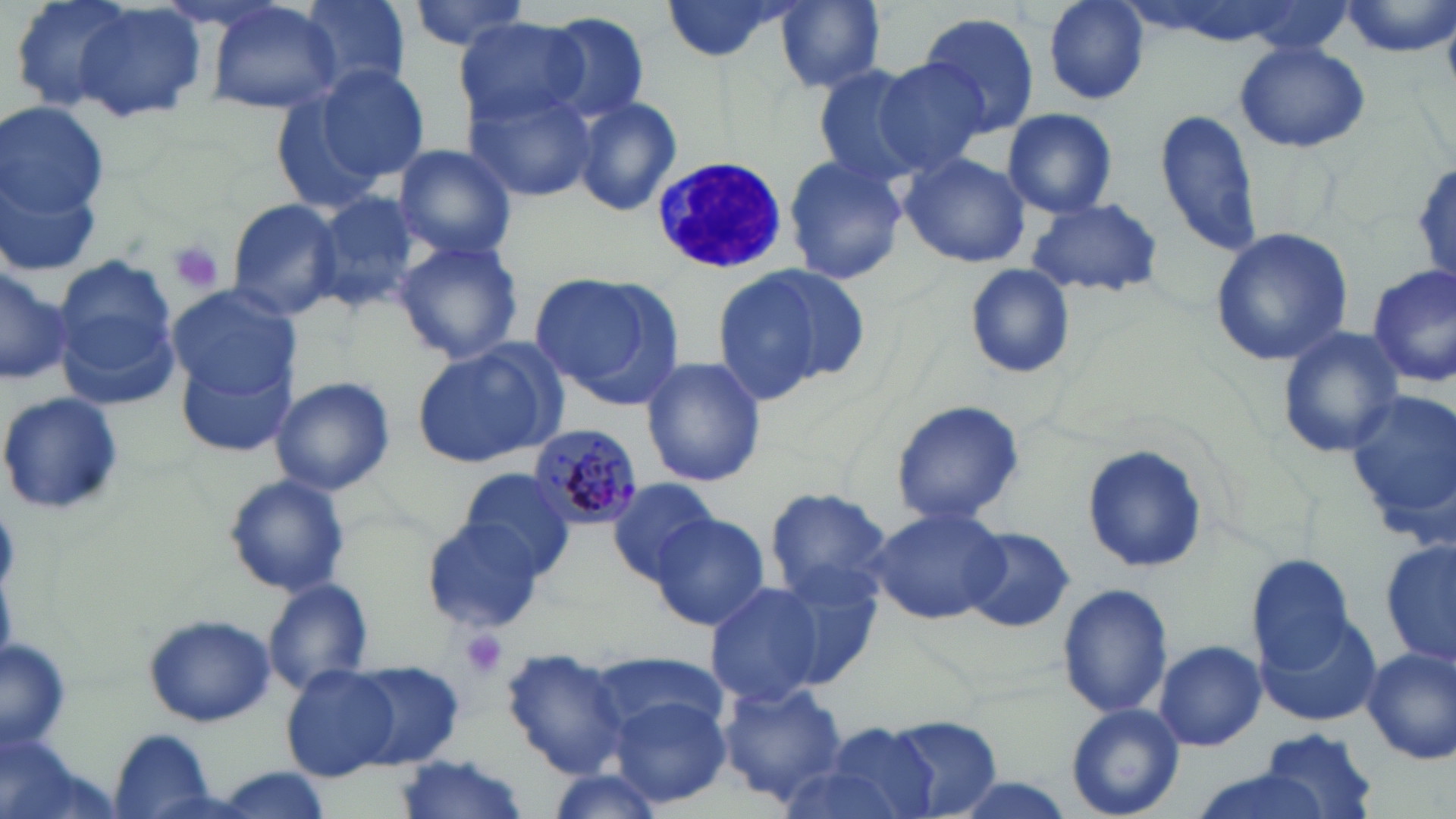
slide-level diagnosis = Plasmodium malariae
stain = May-Grünwald-Giemsa
modality = optical microscopy
field of view = one of a larger specimen
Plasmodium malariae-infected red blood cell locations = approximate bounding boxes as named x1/y1/x2/y2 corners in pixels: (x1=525, y1=421, x2=645, y2=528)
image size = 1456×819 pixels
magnification = 1000x
platelet locations = approximate bounding boxes as named x1/y1/x2/y2 corners in pixels: (x1=168, y1=241, x2=226, y2=294), (x1=458, y1=628, x2=510, y2=681)
uninfected red blood cell locations = approximate bounding boxes as named x1/y1/x2/y2 corners in pixels: (x1=37, y1=0, x2=210, y2=129), (x1=294, y1=0, x2=412, y2=96), (x1=404, y1=0, x2=533, y2=52), (x1=658, y1=0, x2=795, y2=61), (x1=1043, y1=0, x2=1150, y2=104), (x1=774, y1=1, x2=887, y2=91), (x1=1342, y1=1, x2=1454, y2=57), (x1=204, y1=2, x2=341, y2=116), (x1=538, y1=12, x2=652, y2=128), (x1=917, y1=13, x2=1042, y2=136), (x1=454, y1=22, x2=585, y2=125), (x1=1233, y1=39, x2=1371, y2=152), (x1=869, y1=59, x2=991, y2=175), (x1=305, y1=63, x2=431, y2=188), (x1=812, y1=67, x2=929, y2=182), (x1=465, y1=87, x2=596, y2=202), (x1=572, y1=97, x2=682, y2=216), (x1=0, y1=104, x2=112, y2=220), (x1=1155, y1=107, x2=1264, y2=257), (x1=1001, y1=108, x2=1119, y2=218), (x1=393, y1=143, x2=519, y2=261), (x1=0, y1=151, x2=106, y2=281), (x1=899, y1=153, x2=1030, y2=269), (x1=783, y1=154, x2=909, y2=284), (x1=1409, y1=161, x2=1456, y2=281), (x1=312, y1=190, x2=423, y2=314), (x1=1026, y1=197, x2=1166, y2=296), (x1=225, y1=199, x2=343, y2=320), (x1=1207, y1=225, x2=1355, y2=366), (x1=393, y1=240, x2=524, y2=365), (x1=53, y1=254, x2=182, y2=397), (x1=1366, y1=262, x2=1456, y2=386), (x1=0, y1=264, x2=71, y2=387), (x1=964, y1=264, x2=1075, y2=380), (x1=711, y1=265, x2=860, y2=401), (x1=530, y1=270, x2=685, y2=406), (x1=166, y1=286, x2=299, y2=400), (x1=1277, y1=327, x2=1405, y2=460), (x1=173, y1=342, x2=300, y2=459), (x1=411, y1=343, x2=557, y2=466), (x1=640, y1=356, x2=766, y2=487), (x1=270, y1=376, x2=395, y2=497), (x1=1339, y1=392, x2=1456, y2=525), (x1=0, y1=393, x2=125, y2=516), (x1=890, y1=399, x2=1026, y2=529), (x1=1081, y1=443, x2=1208, y2=575), (x1=457, y1=466, x2=577, y2=579), (x1=223, y1=471, x2=351, y2=598), (x1=606, y1=477, x2=722, y2=584), (x1=765, y1=485, x2=893, y2=606), (x1=869, y1=505, x2=1010, y2=624), (x1=649, y1=511, x2=769, y2=632), (x1=424, y1=518, x2=546, y2=632), (x1=960, y1=527, x2=1074, y2=633), (x1=1380, y1=538, x2=1456, y2=669), (x1=1246, y1=553, x2=1356, y2=670), (x1=762, y1=565, x2=884, y2=690), (x1=262, y1=577, x2=371, y2=693), (x1=704, y1=578, x2=836, y2=710), (x1=1058, y1=583, x2=1173, y2=720), (x1=1257, y1=611, x2=1383, y2=727), (x1=145, y1=614, x2=276, y2=728), (x1=2, y1=638, x2=71, y2=751), (x1=1154, y1=640, x2=1267, y2=752), (x1=1361, y1=647, x2=1455, y2=767), (x1=500, y1=648, x2=632, y2=778), (x1=587, y1=648, x2=729, y2=740), (x1=345, y1=660, x2=466, y2=769), (x1=281, y1=665, x2=402, y2=782), (x1=717, y1=682, x2=850, y2=806), (x1=607, y1=696, x2=729, y2=808), (x1=1065, y1=705, x2=1182, y2=818), (x1=880, y1=716, x2=1002, y2=818), (x1=823, y1=724, x2=937, y2=819), (x1=1259, y1=727, x2=1377, y2=817), (x1=107, y1=731, x2=220, y2=818), (x1=392, y1=754, x2=532, y2=819), (x1=1182, y1=771, x2=1340, y2=819)
preparation = thin blood film
white blood cell locations = approximate bounding boxes as named x1/y1/x2/y2 corners in pixels: (x1=648, y1=154, x2=795, y2=279)